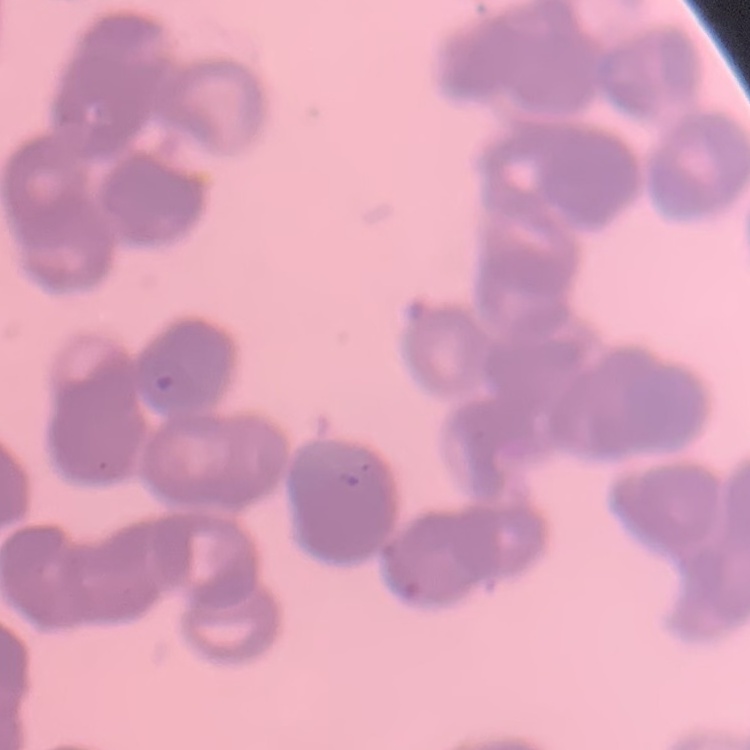
The erythrocytes exhibit rouleaux formation. Square crop of a larger photomicrograph. Thin blood smear. Field's or Giemsa stain.